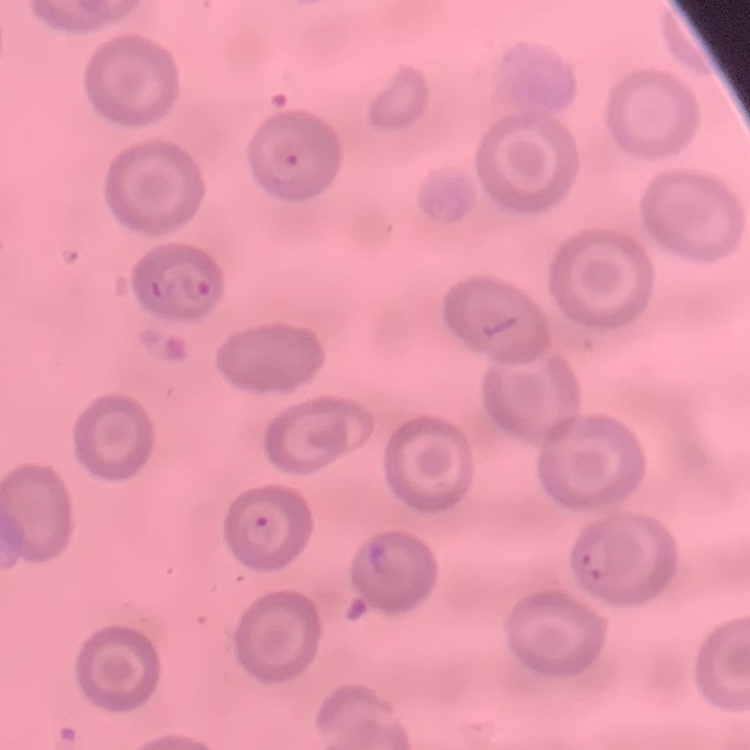
The erythrocytes exhibit no rouleaux formation. Thin blood film. Square crop of a larger photomicrograph. Stained with either Field's or Giemsa.